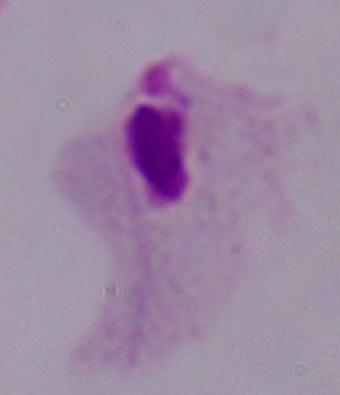 Photomicrograph. A trichomonad is shown. 1000x magnification.